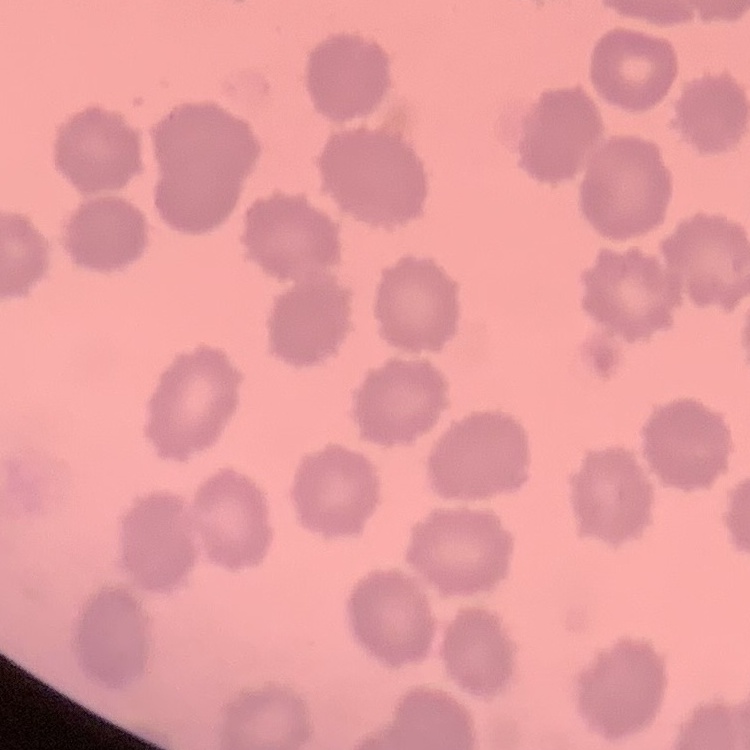

Summary:
  - Red blood cell morphology: no rouleaux formation
  - Image type: square crop of a larger photomicrograph
  - Preparation: thin peripheral smear
  - Stain: Field's or Giemsa